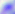

Toxoplasma gondii is shown. Photomicrograph. 400x magnification.